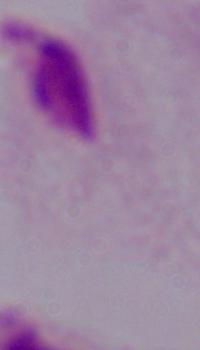

Summary:
  - Modality: micrograph
  - Identification: trichomonad
  - Magnification: 1000x